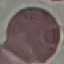

Summary:
  - Malaria status: uninfected
  - Image type: automatically extracted cell patch, resized to 64 × 64 pixels
  - Capture: smartphone through the microscope eyepiece
  - Preparation: thin blood film
  - Stain: Giemsa